Report the malaria status of this cell.
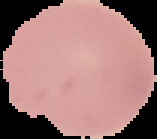

It is uninfected.

Summary:
  - Preparation: thin blood smear
  - Image size: 157×139 pixels
  - Image type: cell region segmented out of the field of view; surrounding area masked to black